Report the malaria status of this cell.
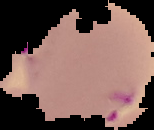

It is parasitized.

From a thin blood smear. Image is 154×130 pixels. Segmented cell region on a black background.